State the preparation type.
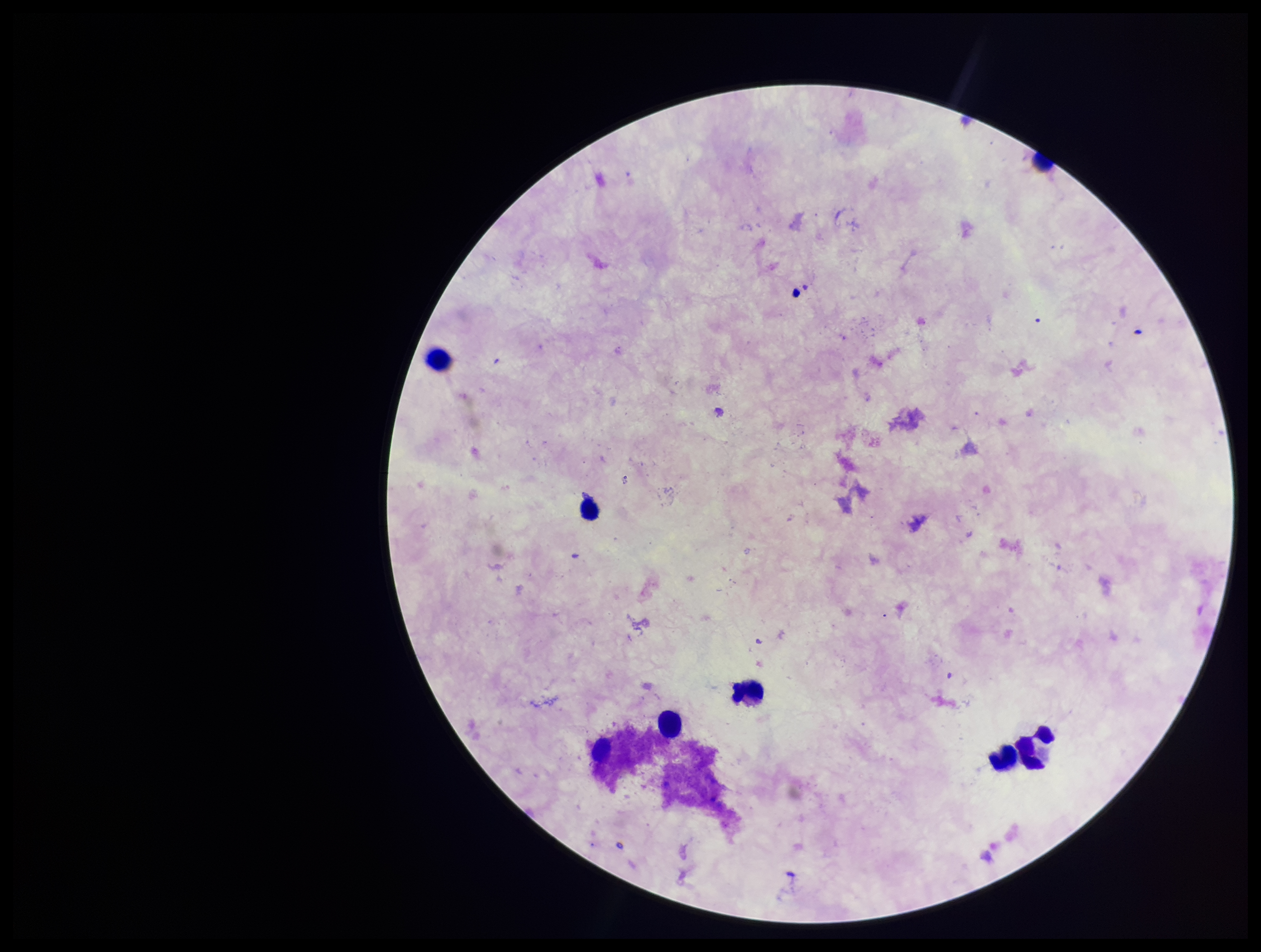

A thick smear.

leukocyte count = 7
stain = Giemsa
patient malaria status = negative
parasite count = 0
Plasmodium parasites = none identified
field of view = single
capture = smartphone photograph through the microscope eyepiece
image size = 1261×952 pixels